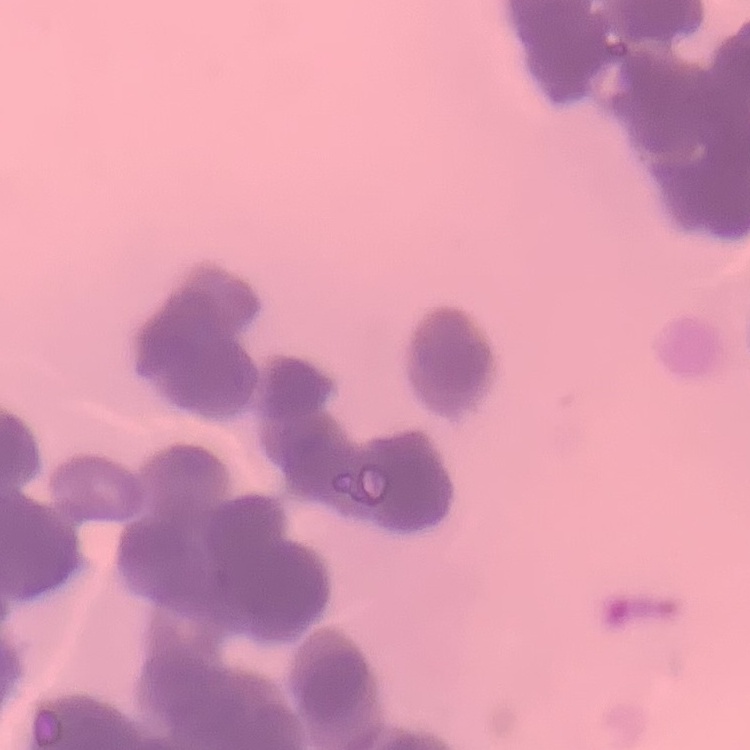

Summary:
  - Red blood cell morphology: rouleaux formation
  - Preparation: thin blood smear
  - Image type: one tile cut from a larger photomicrograph
  - Stain: Field's or Giemsa